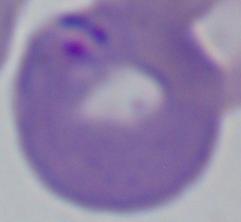
Summary:
  - Modality: micrograph
  - Identification: Babesia
  - Magnification: 1000x